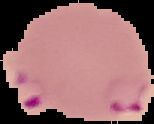 Image is 154×124 pixels. Result: Plasmodium parasites identified. Segmented cell region on a black background. From a thin blood film.